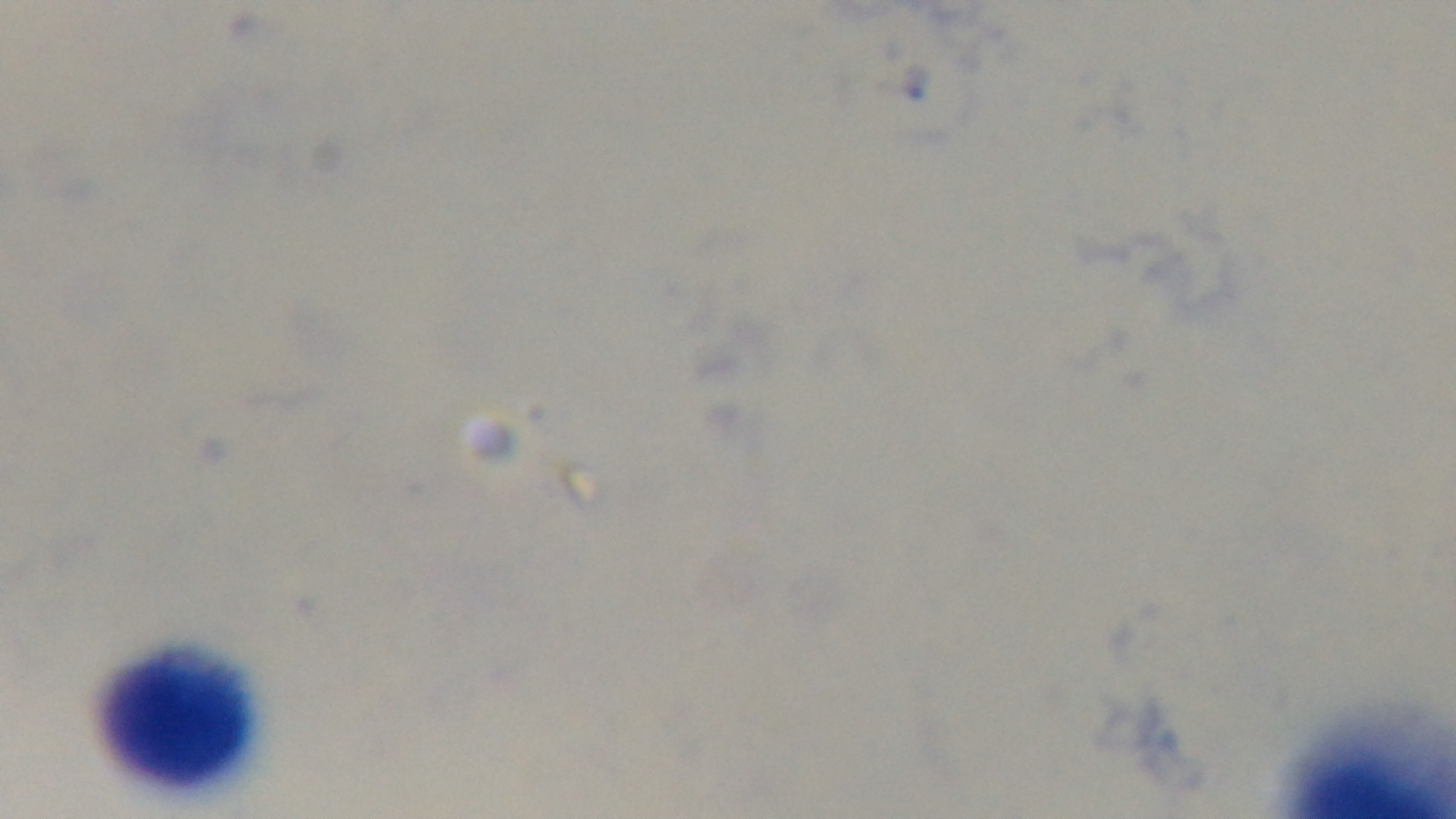

Preparation: thick blood film. Malaria status: negative. Mounted 4K digital camera. Single field of view. Light microscopy. Oil-immersion objective, 100x. Giemsa-stained.